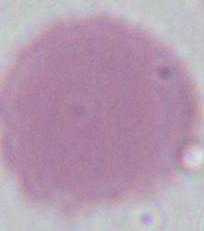

Summary:
  - Magnification: 1000x
  - Modality: micrograph
  - Identification: erythrocyte